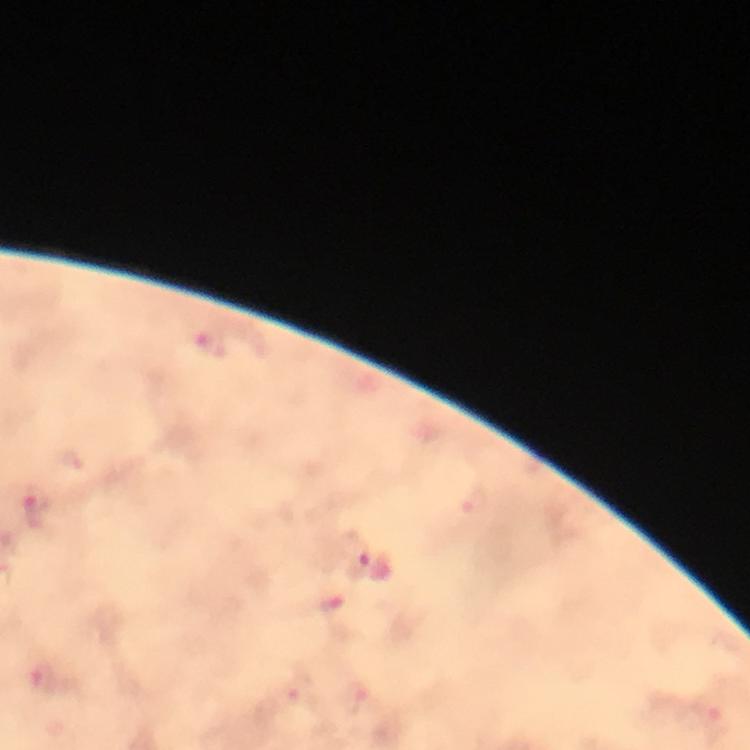
Approximate centers as [x, y] in pixels. Plasmodium parasite locations: [209, 347], [38, 503], [355, 556], [43, 680], [715, 726]. Immersion oil applied. Image is 750×750 pixels. Photographed through the microscope with a smartphone camera. From a malaria diagnostic workup. Thick blood smear. A crop from one field of view. Giemsa-stained preparation. 100x magnification.